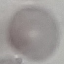

Result: negative for malaria parasites. Automatically extracted cell patch, resized to 64 × 64 pixels. Giemsa stain. Thin blood film. Acquired by smartphone through the microscope eyepiece.